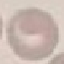

malaria status = uninfected
stain = Giemsa
capture = smartphone camera at the microscope eyepiece
image type = automatically extracted cell patch, resized to 64 × 64 pixels
preparation = thin smear